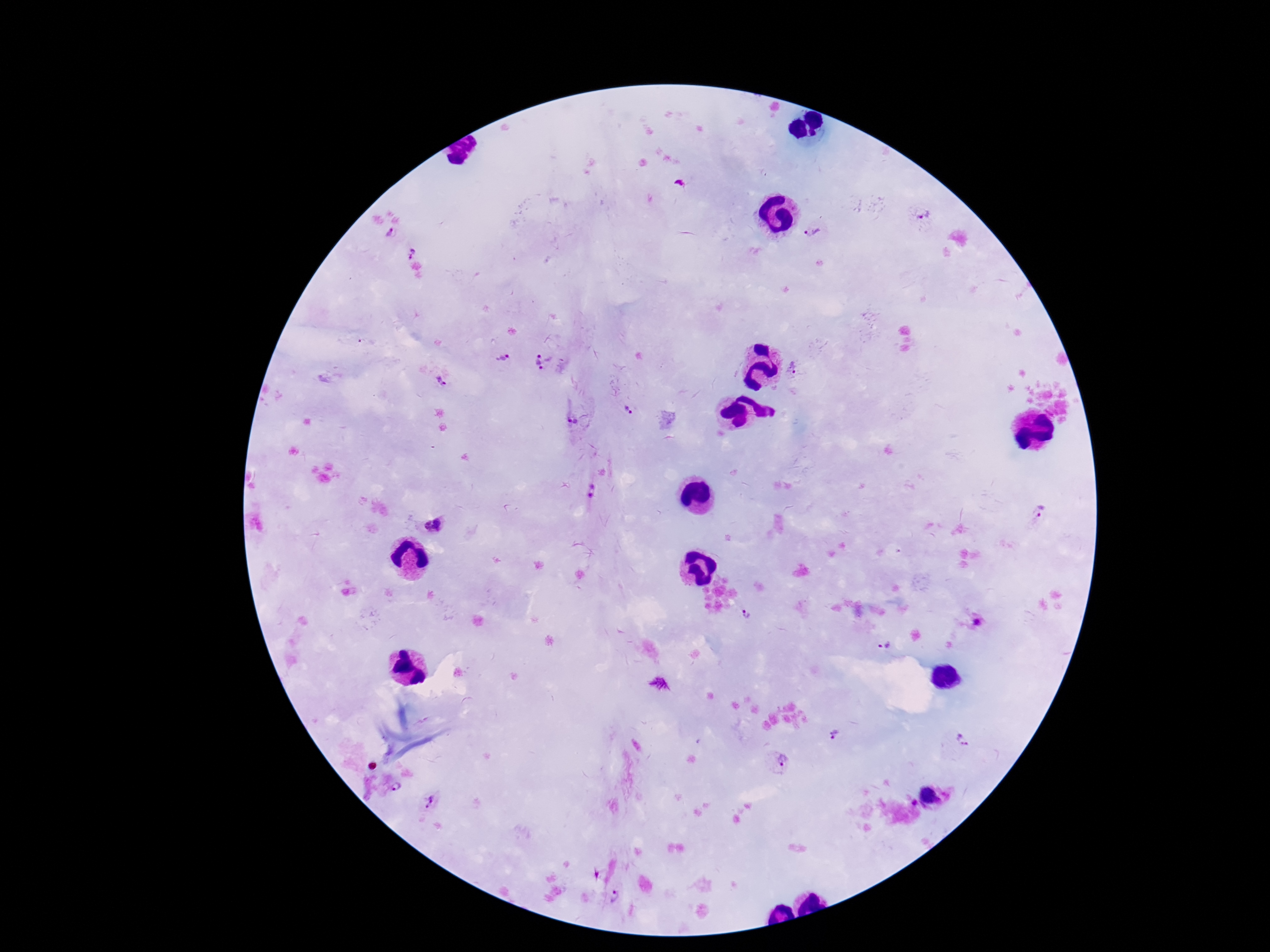

Approximate centers as [x, y] in pixels. Plasmodium parasite locations: [924, 214], [392, 233], [813, 233], [413, 253], [503, 359], [544, 363], [794, 367], [442, 382], [628, 412], [574, 420], [591, 490], [1037, 521], [435, 526], [745, 616], [978, 623], [885, 647], [660, 684], [837, 735], [963, 741], [785, 766], [397, 788], [928, 797], [432, 803], [617, 897]. Image is 1270×952 pixels. Giemsa stain. Patient malaria status: positive. Smartphone photograph taken through the microscope eyepiece. Single field of view. Thick blood film. 100x magnification.